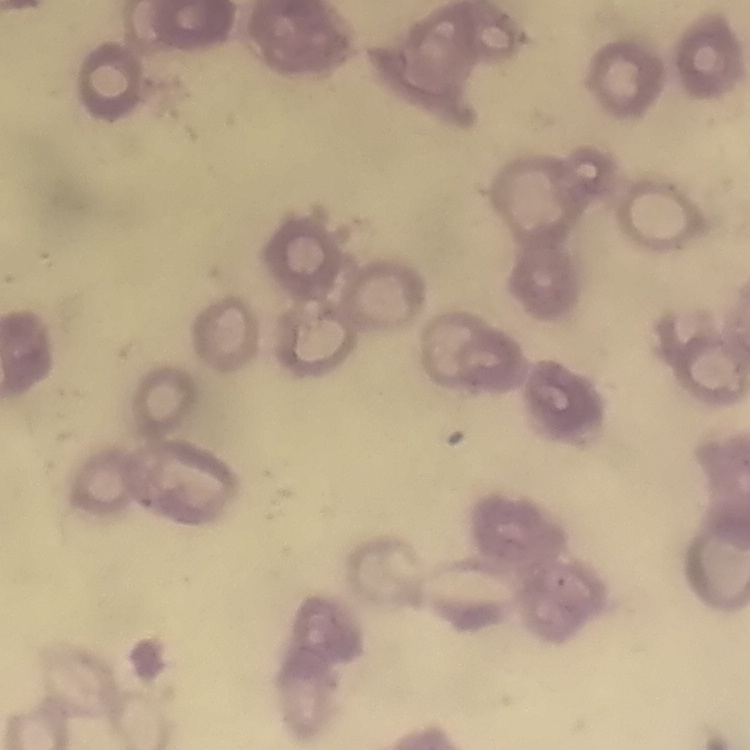
erythrocyte_morphology: rouleaux formation
preparation: thin blood smear
stain: Field's or Giemsa
image_type: one tile cut from a larger photomicrograph